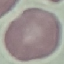
Malaria status: uninfected. Giemsa-stained preparation. Acquired by smartphone through the microscope eyepiece. Cell patch, automatically extracted from a larger field of view and resized to 64 × 64 pixels. Thin smear of blood.